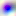 400x magnification. Toxoplasma gondii is seen. Micrograph.